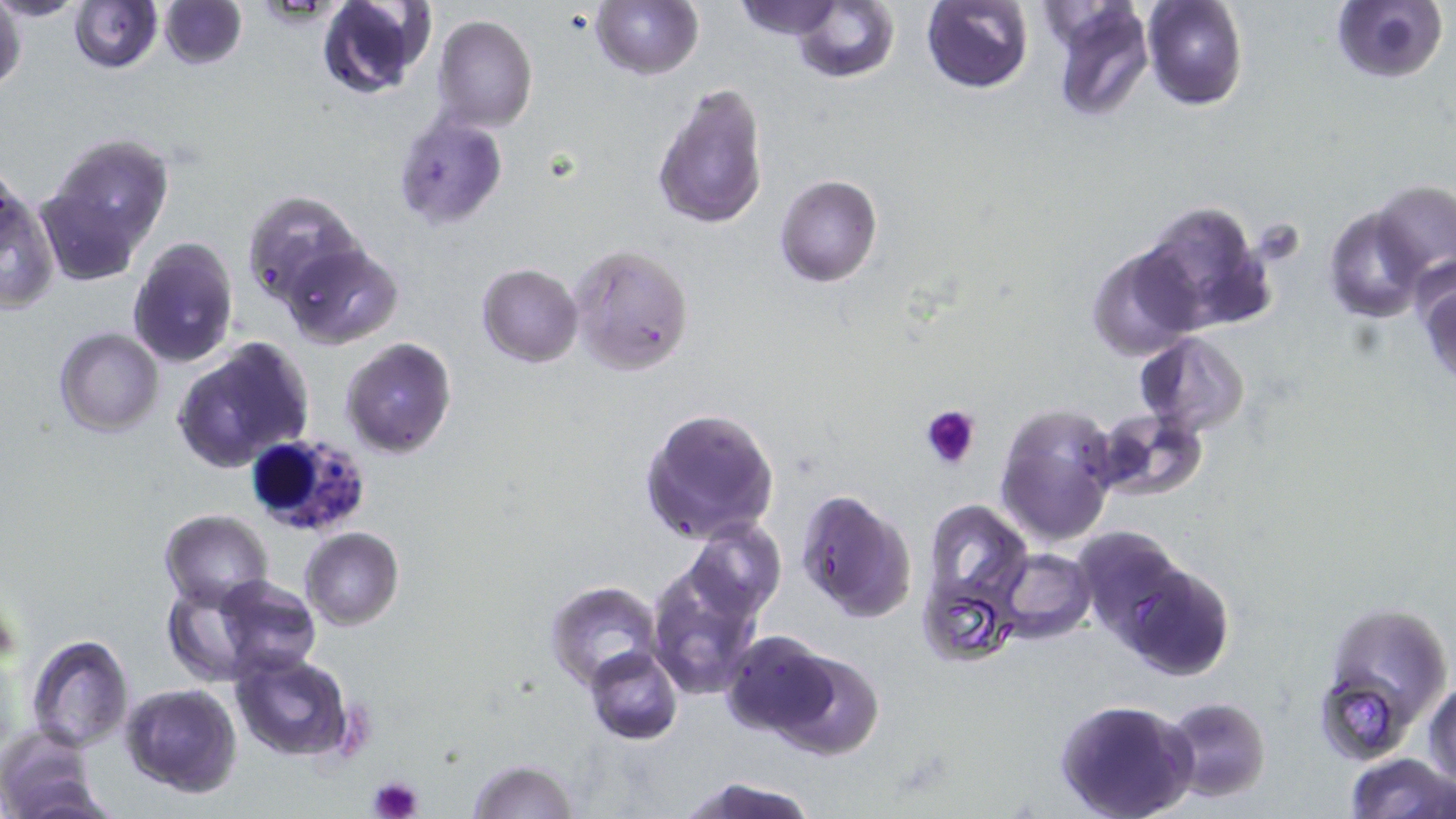
slide-level diagnosis = Plasmodium falciparum
platelet locations = approximate bounding boxes as named x1/y1/x2/y2 corners in pixels: (x1=919, y1=403, x2=980, y2=471), (x1=368, y1=777, x2=423, y2=819)
modality = optical microscopy
stain = May-Grünwald-Giemsa
white blood cell locations = approximate bounding boxes as named x1/y1/x2/y2 corners in pixels: (x1=244, y1=432, x2=371, y2=538)
field of view = one of a larger specimen
preparation = thin blood smear
image size = 1456×819 pixels
magnification = 1000x
uninfected red blood cell locations = approximate bounding boxes as named x1/y1/x2/y2 corners in pixels: (x1=0, y1=0, x2=27, y2=100), (x1=0, y1=0, x2=88, y2=20), (x1=158, y1=0, x2=247, y2=69), (x1=314, y1=0, x2=433, y2=100), (x1=590, y1=0, x2=703, y2=80), (x1=1142, y1=0, x2=1247, y2=110), (x1=1330, y1=0, x2=1447, y2=85), (x1=69, y1=1, x2=161, y2=73), (x1=731, y1=1, x2=846, y2=40), (x1=790, y1=1, x2=900, y2=86), (x1=922, y1=1, x2=1033, y2=93), (x1=1047, y1=5, x2=1154, y2=122), (x1=433, y1=14, x2=538, y2=133), (x1=653, y1=81, x2=769, y2=232), (x1=393, y1=116, x2=508, y2=228), (x1=50, y1=136, x2=174, y2=248), (x1=775, y1=175, x2=883, y2=288), (x1=1, y1=179, x2=58, y2=314), (x1=1372, y1=179, x2=1456, y2=279), (x1=35, y1=185, x2=142, y2=285), (x1=243, y1=190, x2=364, y2=310), (x1=1138, y1=199, x2=1274, y2=333), (x1=1324, y1=205, x2=1429, y2=322), (x1=127, y1=239, x2=239, y2=368), (x1=1086, y1=241, x2=1205, y2=359), (x1=280, y1=242, x2=403, y2=349), (x1=569, y1=243, x2=696, y2=377), (x1=1415, y1=260, x2=1456, y2=389), (x1=477, y1=263, x2=583, y2=366), (x1=55, y1=327, x2=162, y2=435), (x1=1135, y1=332, x2=1251, y2=437), (x1=169, y1=336, x2=316, y2=472), (x1=340, y1=337, x2=455, y2=458), (x1=996, y1=400, x2=1121, y2=550), (x1=639, y1=406, x2=782, y2=546), (x1=1090, y1=410, x2=1207, y2=502), (x1=795, y1=488, x2=917, y2=623), (x1=923, y1=500, x2=1032, y2=607), (x1=160, y1=509, x2=274, y2=609), (x1=685, y1=517, x2=785, y2=622), (x1=1072, y1=525, x2=1193, y2=647), (x1=300, y1=527, x2=404, y2=630), (x1=997, y1=549, x2=1097, y2=641), (x1=215, y1=557, x2=393, y2=661), (x1=1109, y1=558, x2=1237, y2=680), (x1=645, y1=560, x2=763, y2=702), (x1=917, y1=571, x2=1017, y2=666), (x1=212, y1=574, x2=321, y2=678), (x1=547, y1=581, x2=665, y2=690), (x1=160, y1=582, x2=260, y2=685), (x1=1317, y1=599, x2=1452, y2=749), (x1=720, y1=629, x2=841, y2=737), (x1=26, y1=635, x2=134, y2=750), (x1=585, y1=646, x2=683, y2=745), (x1=769, y1=646, x2=886, y2=759), (x1=228, y1=648, x2=356, y2=764), (x1=1425, y1=678, x2=1456, y2=793), (x1=119, y1=684, x2=243, y2=797), (x1=1158, y1=696, x2=1271, y2=804), (x1=1054, y1=698, x2=1199, y2=819), (x1=0, y1=732, x2=104, y2=819), (x1=1342, y1=751, x2=1455, y2=819), (x1=464, y1=759, x2=581, y2=818), (x1=676, y1=776, x2=821, y2=819)